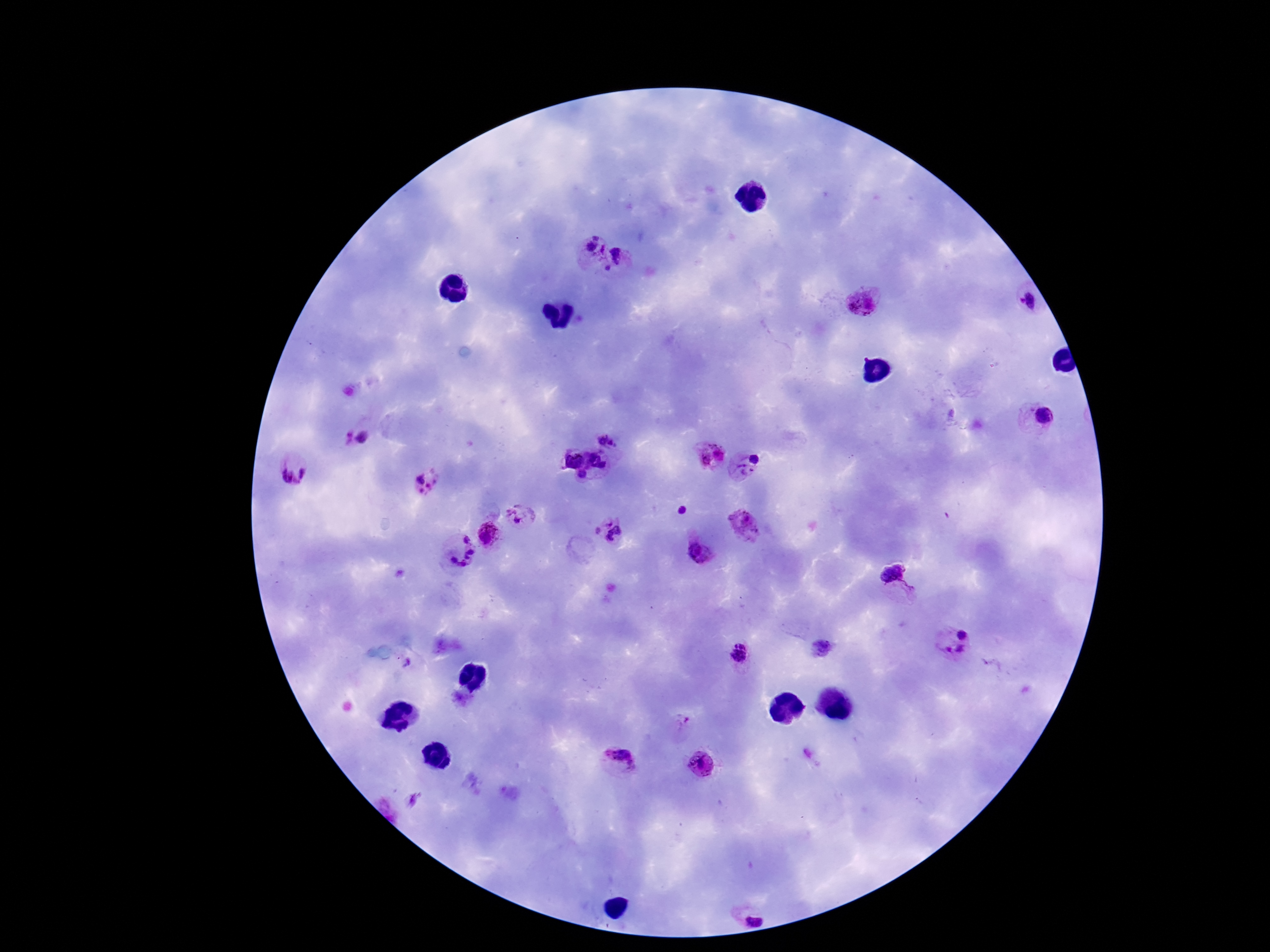 Approximate object centers, in pixels from the top-left corner. Plasmodium parasite locations: (x=594, y=248), (x=623, y=258), (x=864, y=301), (x=1026, y=305), (x=1043, y=414), (x=353, y=436), (x=609, y=437), (x=712, y=453), (x=598, y=456), (x=572, y=458), (x=747, y=464), (x=294, y=473), (x=583, y=476), (x=429, y=481), (x=682, y=511), (x=520, y=518), (x=745, y=525), (x=610, y=530), (x=487, y=536), (x=697, y=549), (x=459, y=551), (x=895, y=582), (x=963, y=633), (x=956, y=650), (x=739, y=654), (x=684, y=725), (x=618, y=762), (x=700, y=763), (x=753, y=909). Patient malaria status: infected. Smartphone photograph taken through the microscope eyepiece. 100x magnification. Image is 1270×952 pixels. Single field of view. Giemsa stain. Thick blood smear.